Report the malaria status of this cell.
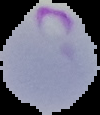
It is parasitized.

{
  "preparation": "thin blood film",
  "image_size": "100×115 pixels",
  "image_type": "segmented cell region with the area outside set to black"
}